Report the malaria status of this cell.
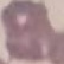
It is uninfected.

Summary:
  - Preparation: thin blood film
  - Capture: smartphone camera at the microscope eyepiece
  - Image type: automatically extracted cell patch, resized to 64 × 64 pixels
  - Stain: Giemsa